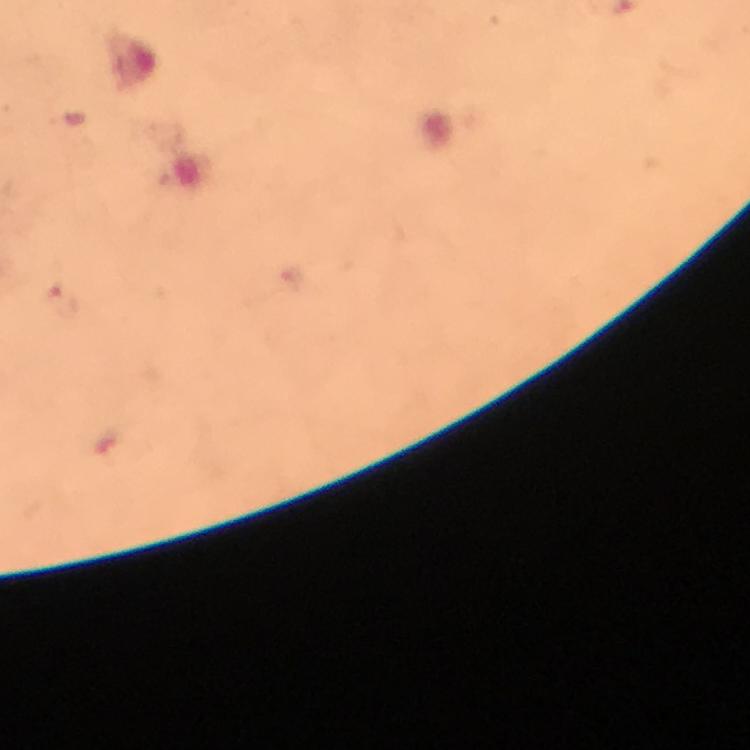

Approximate object centers, in pixels from the top-left corner. Plasmodium parasite locations: (x=60, y=302). Image is 750×750 pixels. From a diagnostic examination for malaria. Cropped region of a single field of view. Giemsa-stained preparation. Immersion oil applied. Photographed with a smartphone mounted on the microscope. At 100x magnification. Thick blood smear.